Identify the cell.
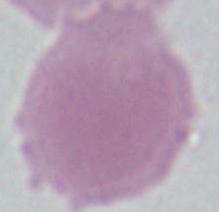
An erythrocyte.

Summary:
  - Modality: micrograph
  - Magnification: 1000x